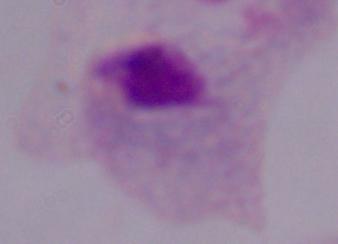

Photomicrograph. A trichomonad is shown. Captured at 1000x magnification.